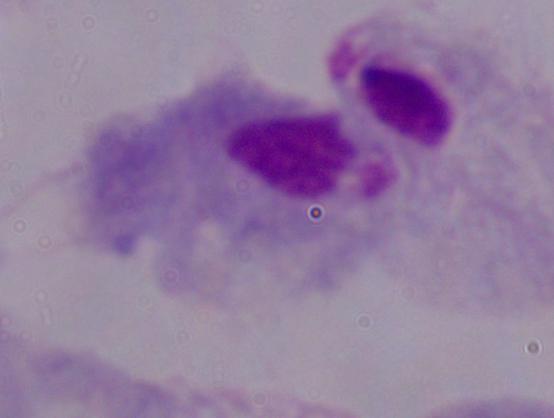
identification: trichomonad
magnification: 1000x
modality: photomicrograph